Outline platelets.
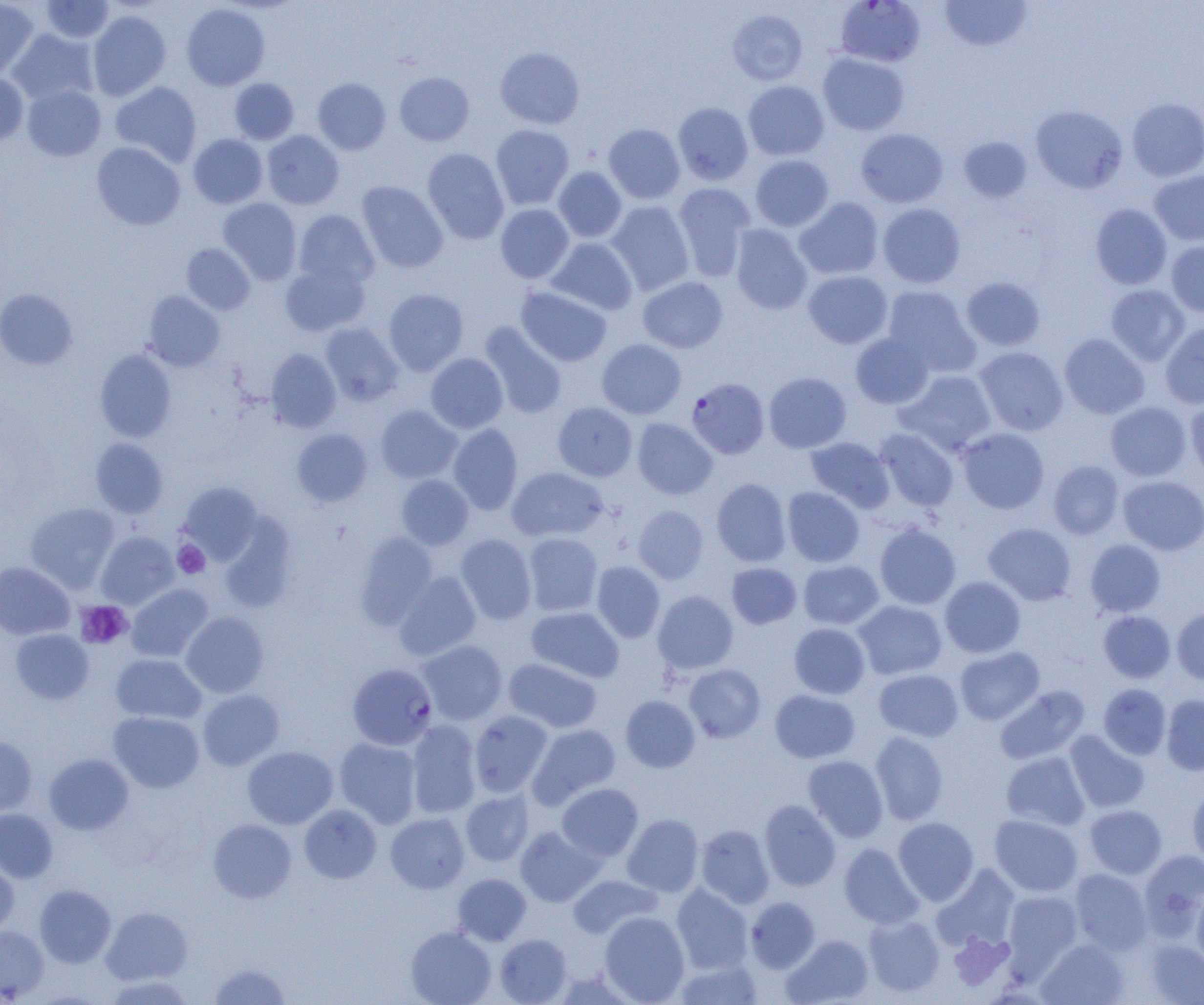
Approximate bounding boxes as (x1,y1)-(x2,y2) corner pairs in pixels.
Platelets: (173,541)-(210,579), (76,600)-(132,649).

Summary:
  - Uninfected red blood cell locations: (0,0)-(39,79), (40,0)-(114,43), (940,1)-(1032,52), (181,3)-(270,90), (727,8)-(808,86), (87,10)-(171,101), (8,28)-(98,106), (495,47)-(585,129), (817,52)-(909,136), (0,71)-(29,145), (394,72)-(474,146), (229,78)-(299,145), (312,78)-(391,154), (743,80)-(830,161), (110,81)-(202,167), (22,84)-(106,161), (1127,98)-(1204,181), (672,102)-(753,185), (1031,105)-(1128,194), (603,123)-(685,204), (490,124)-(574,210), (855,128)-(948,209), (262,130)-(344,209), (188,134)-(268,209), (958,136)-(1032,202), (91,142)-(185,230), (422,148)-(509,244), (750,154)-(834,232), (553,166)-(626,243), (1148,170)-(1204,246), (357,181)-(448,273), (673,183)-(756,280), (218,197)-(302,285), (794,197)-(884,280), (606,201)-(694,295), (877,203)-(966,288), (1090,203)-(1172,290), (495,204)-(574,283), (293,209)-(379,290), (729,224)-(813,315), (546,237)-(637,315), (1166,240)-(1204,318), (181,243)-(255,315), (280,260)-(371,336), (803,270)-(892,348), (637,276)-(728,353), (961,277)-(1045,351), (1106,284)-(1190,366), (882,285)-(980,377), (516,286)-(612,366), (0,288)-(78,369), (383,288)-(469,375), (143,291)-(224,371), (320,322)-(404,406), (1160,322)-(1204,409), (480,323)-(568,419), (850,332)-(934,409), (1059,333)-(1149,419), (596,338)-(687,419), (974,346)-(1069,436), (95,349)-(177,442), (265,349)-(341,432), (425,353)-(508,433), (896,369)-(997,456), (763,371)-(852,453), (1185,400)-(1204,483), (552,401)-(637,481), (1105,401)-(1192,481), (375,405)-(462,483), (632,418)-(717,499), (448,424)-(523,515), (957,427)-(1050,514), (291,428)-(373,507), (874,428)-(959,512), (805,437)-(894,512), (90,438)-(168,518), (1048,460)-(1124,539), (506,467)-(608,542), (396,475)-(474,550), (1118,476)-(1204,555), (711,478)-(791,566), (178,482)-(262,563), (782,487)-(865,567), (25,502)-(120,592), (633,505)-(708,584), (220,517)-(296,613), (874,523)-(961,609), (983,523)-(1076,606), (95,531)-(179,610), (355,532)-(438,628), (523,532)-(603,616), (455,533)-(537,624), (1085,539)-(1165,617), (798,560)-(884,630), (591,561)-(665,642), (0,562)-(75,640), (726,562)-(801,629), (394,571)-(482,660), (939,576)-(1026,658), (126,583)-(214,662), (653,590)-(738,674), (853,600)-(947,680), (526,606)-(623,682), (1172,606)-(1204,685), (1098,611)-(1175,683), (181,612)-(269,698), (788,623)-(870,699), (10,629)-(94,704), (417,640)-(508,725), (954,646)-(1044,725), (111,653)-(206,724), (503,657)-(602,733), (684,664)-(766,743), (874,668)-(963,742), (1098,683)-(1172,759), (995,685)-(1089,765), (197,689)-(284,770), (770,689)-(860,763), (1161,694)-(1204,775), (620,695)-(700,773), (469,710)-(552,798), (109,711)-(204,792), (406,721)-(481,818), (528,724)-(621,808), (1065,730)-(1150,813), (870,731)-(949,825), (0,735)-(37,816), (334,737)-(422,828), (242,746)-(338,828), (1001,751)-(1090,831), (43,753)-(133,835), (803,755)-(888,842), (557,783)-(643,861), (1188,787)-(1204,869), (460,790)-(534,866), (759,800)-(840,890), (299,804)-(381,883), (1085,804)-(1167,879), (0,809)-(57,883), (385,813)-(469,893), (622,814)-(703,896), (989,814)-(1083,897), (893,817)-(979,905), (208,819)-(296,903), (695,824)-(774,908), (515,826)-(602,906), (839,843)-(924,929), (1139,849)-(1204,938), (0,855)-(19,939), (933,865)-(1020,952), (1069,869)-(1152,954), (453,874)-(531,945), (567,874)-(661,938), (34,884)-(116,967), (671,884)-(754,973), (1002,890)-(1082,973), (1192,891)-(1204,968), (745,897)-(820,973), (101,906)-(193,985), (599,911)-(690,1004), (863,915)-(945,997), (0,926)-(49,1002), (405,926)-(496,1005), (495,934)-(571,1004), (782,935)-(874,1005), (1037,938)-(1129,1005), (1143,938)-(1204,1004), (674,958)-(764,1004), (209,962)-(290,1004)
  - Plasmodium falciparum-infected red blood cell locations: (829,0)-(918,66), (686,376)-(769,458), (352,663)-(441,750)
  - Slide-level diagnosis: Plasmodium falciparum
  - Image size: 1204×1005 pixels
  - Field of view: one of a larger specimen
  - Magnification: 1000x
  - Modality: optical microscopy
  - Preparation: thin blood film